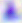

400x magnification. Photomicrograph. Toxoplasma gondii is seen.